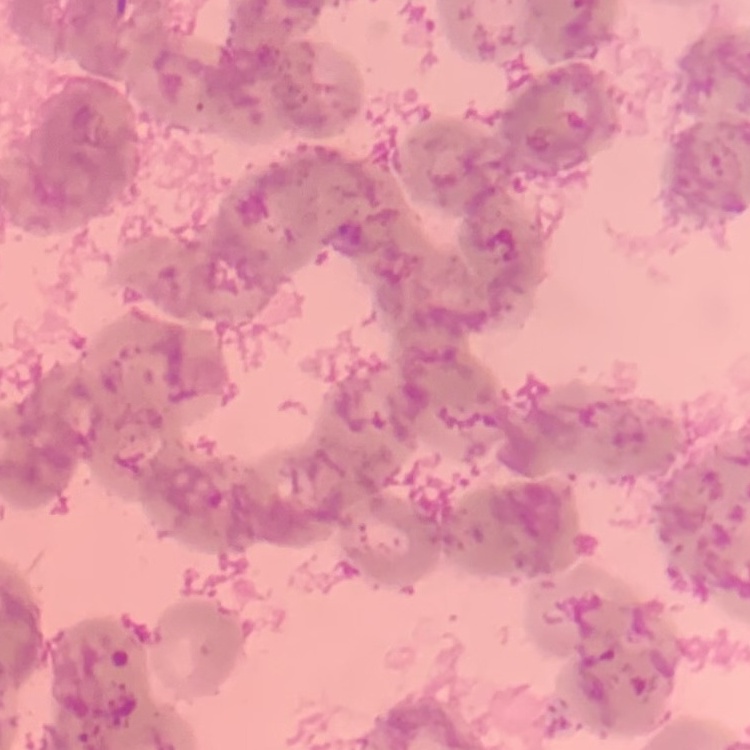
Summary:
  - Red blood cell morphology: rouleaux formation
  - Stain: Field's or Giemsa
  - Image type: one tile cut from a larger photomicrograph
  - Preparation: thin blood film